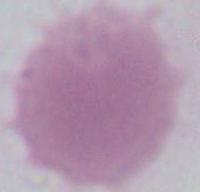 Photomicrograph. An erythrocyte is shown. Captured at 1000x magnification.